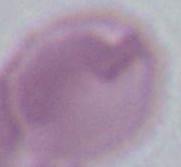
identification = red blood cell
modality = micrograph
magnification = 1000x